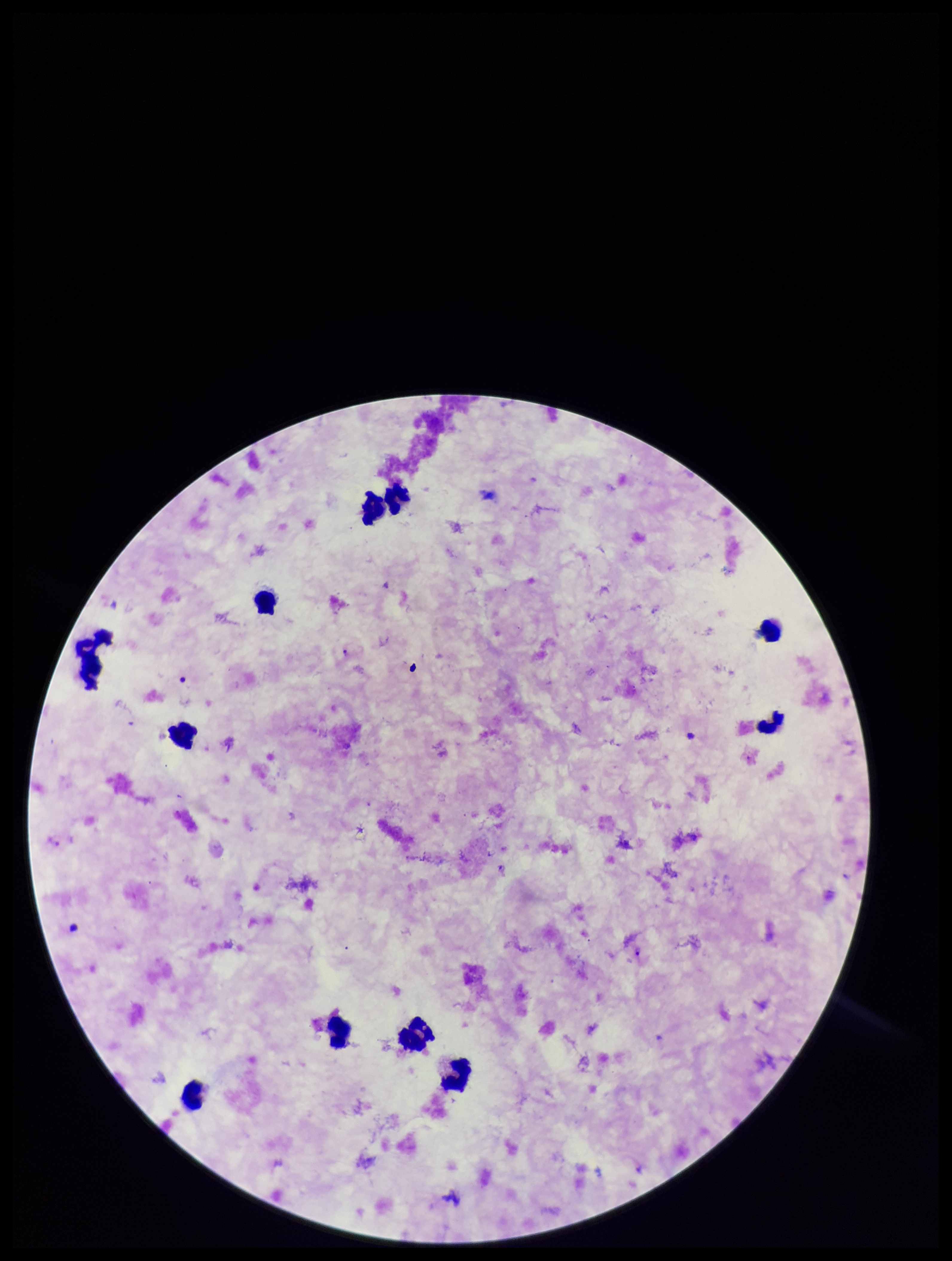 One field from this slide. Plasmodium parasites: seen. Preparation: thick. Patient malaria status: positive. Giemsa stain. Leukocyte count: 11. Image is 952×1261 pixels. Parasite count: 3. Smartphone photograph taken through the eyepiece of a microscope. Species reported for this patient: Plasmodium falciparum.